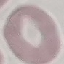
Summary:
  - Malaria status: uninfected
  - Stain: Giemsa
  - Image type: cell patch, automatically extracted from a larger field of view and resized to 64 × 64 pixels
  - Capture: smartphone through the microscope eyepiece
  - Preparation: thin blood smear